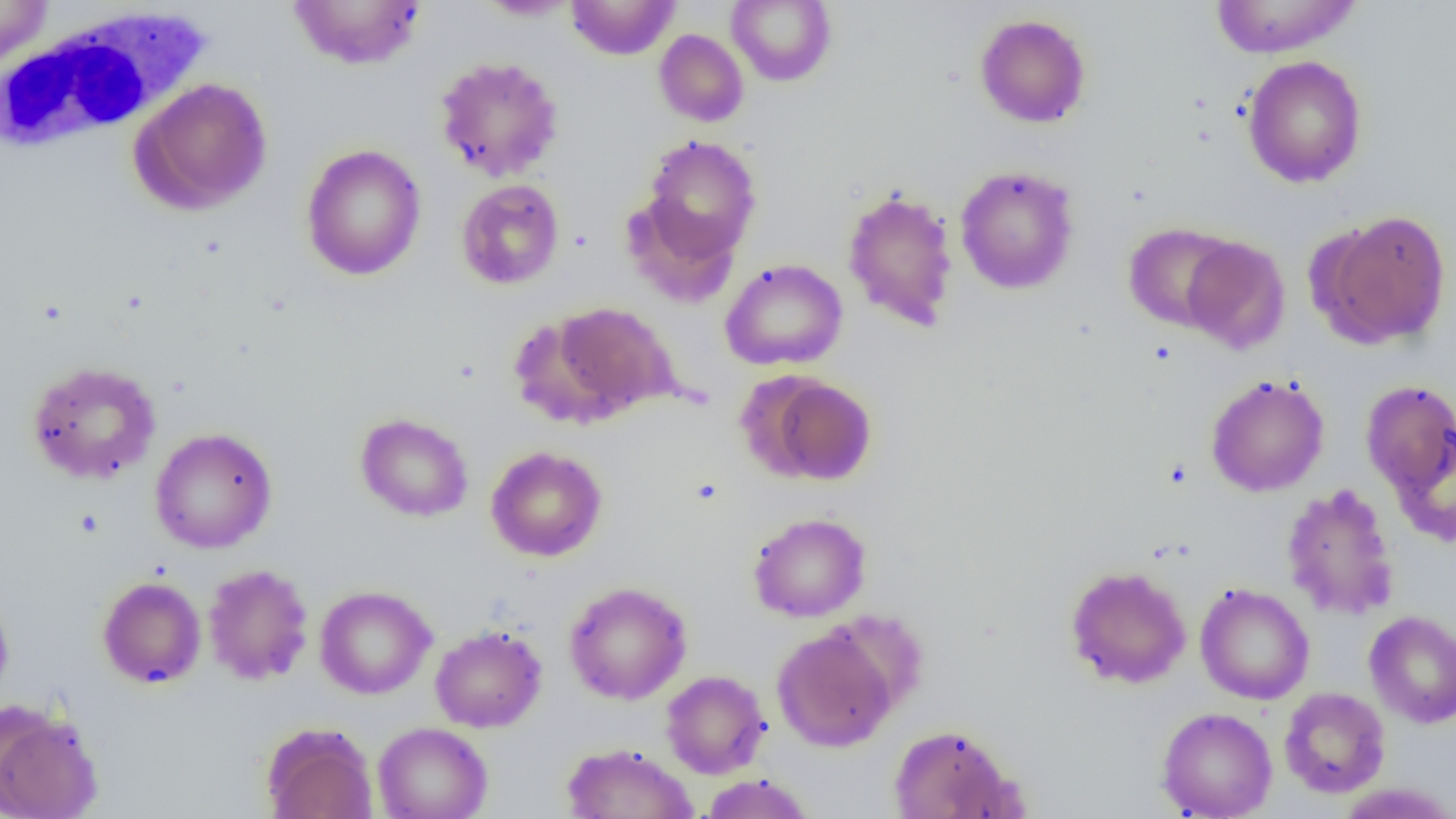
slide-level diagnosis = no evidence of blood parasites
modality = light microscopy
white blood cell locations = approximate bounding boxes as [x1, y1, x2, y2] in pixels: [0, 5, 214, 156]
field of view = one of a larger specimen
uninfected red blood cell locations = approximate bounding boxes as [x1, y1, x2, y2] in pixels: [0, 0, 53, 69], [287, 0, 426, 70], [566, 0, 680, 60], [727, 0, 836, 87], [1209, 0, 1362, 59], [476, 1, 581, 20], [974, 13, 1091, 128], [654, 29, 749, 127], [434, 56, 564, 182], [1242, 56, 1367, 188], [131, 77, 273, 214], [640, 134, 761, 262], [301, 143, 427, 281], [955, 165, 1079, 294], [456, 178, 564, 290], [842, 188, 959, 331], [623, 196, 741, 308], [1317, 210, 1451, 348], [1124, 222, 1240, 332], [1181, 236, 1291, 353], [720, 258, 848, 371], [549, 303, 678, 419], [26, 360, 161, 485], [752, 374, 876, 486], [1205, 374, 1329, 497], [1361, 380, 1456, 499], [355, 413, 474, 522], [149, 427, 277, 553], [1391, 427, 1456, 547], [486, 446, 607, 562], [1281, 483, 1400, 621], [748, 512, 871, 622], [202, 563, 314, 685], [1064, 565, 1191, 689], [97, 576, 207, 689], [564, 581, 692, 704], [1195, 583, 1314, 705], [315, 585, 436, 699], [0, 586, 14, 705], [1364, 610, 1456, 728], [430, 625, 547, 732], [772, 625, 899, 752], [661, 670, 770, 778], [1279, 687, 1391, 798], [0, 700, 103, 819], [1156, 706, 1278, 818], [261, 722, 378, 819], [373, 722, 492, 819], [888, 723, 1023, 818], [561, 742, 697, 819], [699, 774, 817, 818], [1336, 783, 1456, 818]
preparation = thin blood film
image size = 1456×819 pixels
magnification = 1000x